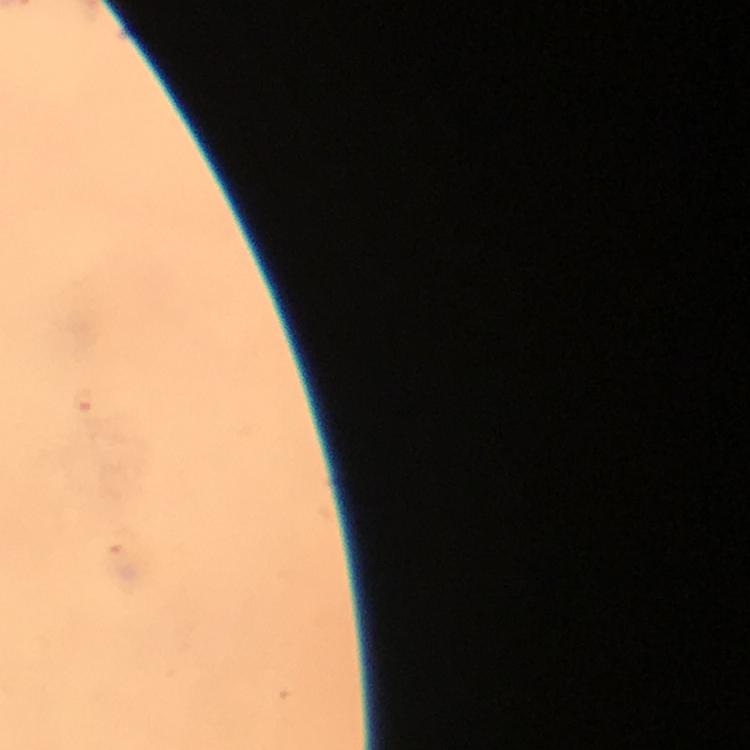
{
  "plasmodium_parasite_locations": "approximate object centers, in pixels from the top-left corner: (x=86, y=402)",
  "image_size": "750×750 pixels",
  "context": "from a malaria diagnostic workup",
  "preparation": "thick blood smear",
  "magnification": "100x",
  "cropped_from": "a single field of view",
  "capture": "smartphone camera through the microscope",
  "immersion_oil": "applied",
  "stain": "Giemsa"
}